Describe the morphology of the erythrocytes.
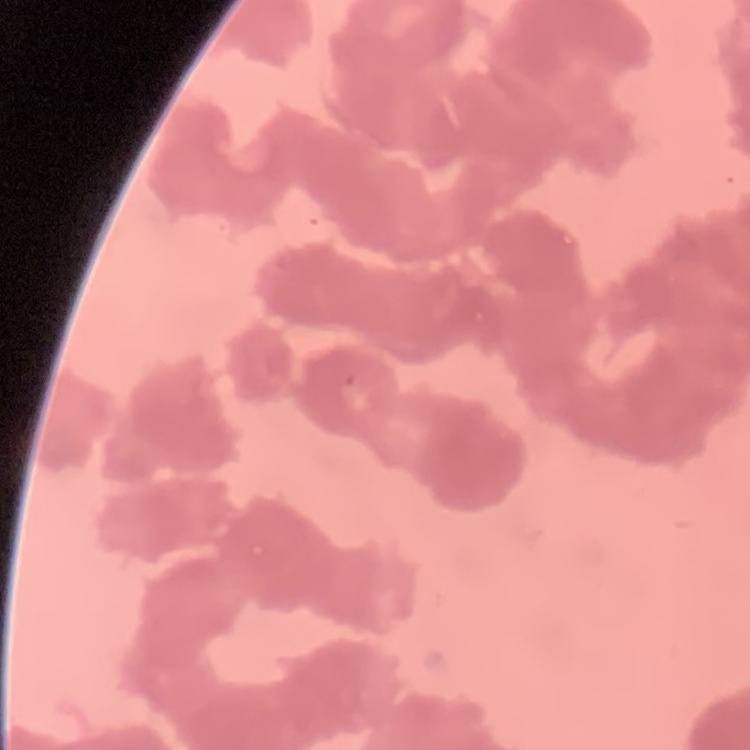

They show rouleaux formation.

image type = square crop of a larger photomicrograph
preparation = thin peripheral smear
stain = Field's or Giemsa